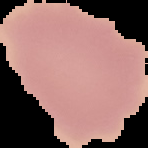

image type = segmented cell region on a black background
image size = 148×148 pixels
result = negative for Plasmodium parasites
preparation = thin blood film